Outline each Plasmodium falciparum-infected red blood cell.
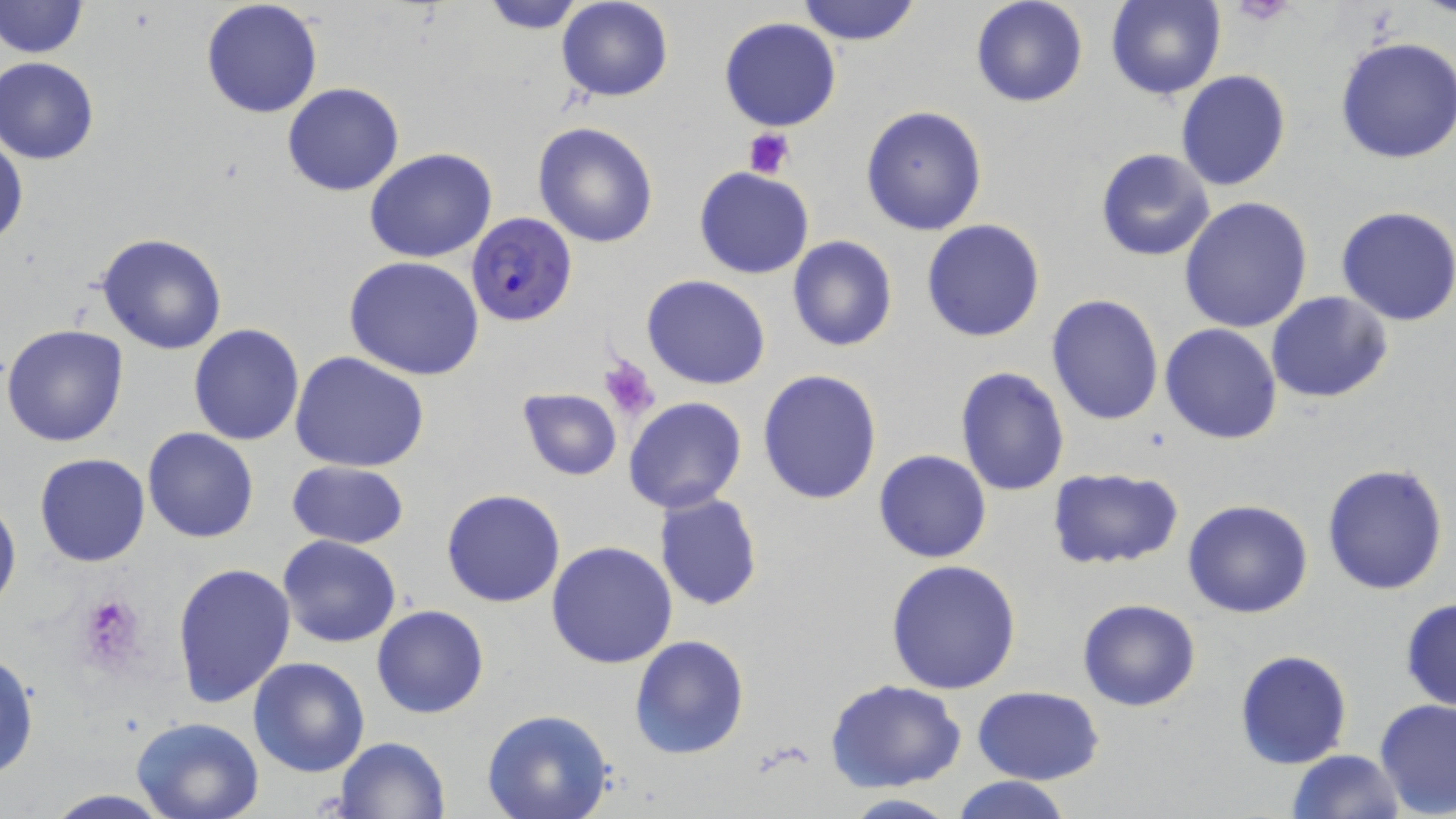
Approximate bounding boxes as (x1,y1)-(x2,y2) corner pairs in pixels.
Plasmodium falciparum-infected red blood cells: (466,212)-(577,327).

Platelet locations: (1230,1)-(1298,29), (745,127)-(795,179), (598,355)-(661,420), (73,592)-(149,675). Uninfected red blood cell locations: (0,0)-(87,60), (201,0)-(324,118), (475,0)-(593,32), (556,0)-(673,102), (970,0)-(1088,108), (1106,0)-(1223,99), (794,1)-(924,47), (718,17)-(842,132), (1334,36)-(1456,164), (2,56)-(100,164), (1175,70)-(1291,193), (281,83)-(404,197), (860,105)-(988,235), (532,122)-(658,248), (1,128)-(26,253), (364,148)-(498,262), (1094,148)-(1215,261), (695,167)-(814,279), (1178,197)-(1314,334), (1336,206)-(1456,326), (920,218)-(1046,343), (96,233)-(229,355), (788,236)-(897,351), (343,255)-(485,380), (641,275)-(770,389), (1267,291)-(1394,403), (1046,295)-(1164,425), (1160,323)-(1284,444), (2,324)-(130,447), (188,324)-(306,446), (289,351)-(432,474), (954,367)-(1071,498), (758,369)-(884,506), (515,387)-(622,481), (623,397)-(748,515), (141,427)-(259,543), (873,449)-(993,564), (34,454)-(152,568), (286,461)-(411,549), (1321,461)-(1450,596), (1047,467)-(1184,570), (440,488)-(566,607), (0,491)-(21,619), (654,494)-(763,611), (1182,499)-(1314,620), (277,536)-(401,649), (546,541)-(678,668), (884,557)-(1024,694), (171,562)-(297,710), (1078,597)-(1200,711), (1399,597)-(1456,711), (371,604)-(489,719), (628,634)-(749,760), (1234,649)-(1353,769), (0,650)-(39,782), (248,656)-(370,777), (826,678)-(967,791), (973,686)-(1104,784), (1374,699)-(1456,818), (481,709)-(616,819), (131,716)-(266,819), (334,736)-(451,818), (1284,749)-(1404,819), (952,776)-(1074,819), (36,789)-(183,819), (837,793)-(962,819). Slide-level diagnosis: Plasmodium falciparum. Thin blood film. Image is 1456×819 pixels. Captured at 1000x magnification. Optical microscopy. May-Grünwald-Giemsa-stained preparation. Single field of view.